Identify the cell.
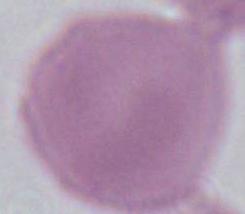
This is an erythrocyte.

Photomicrograph. 1000x magnification.